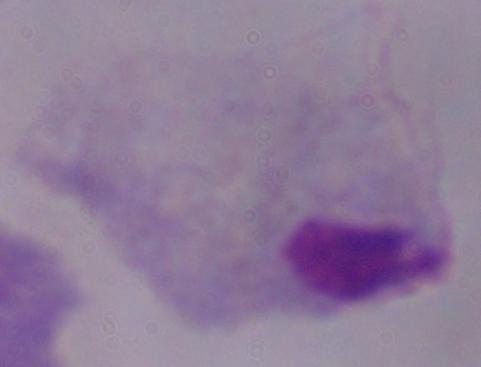
Summary:
  - Magnification: 1000x
  - Modality: micrograph
  - Identification: trichomonad